Give the position of every leukocyte visible.
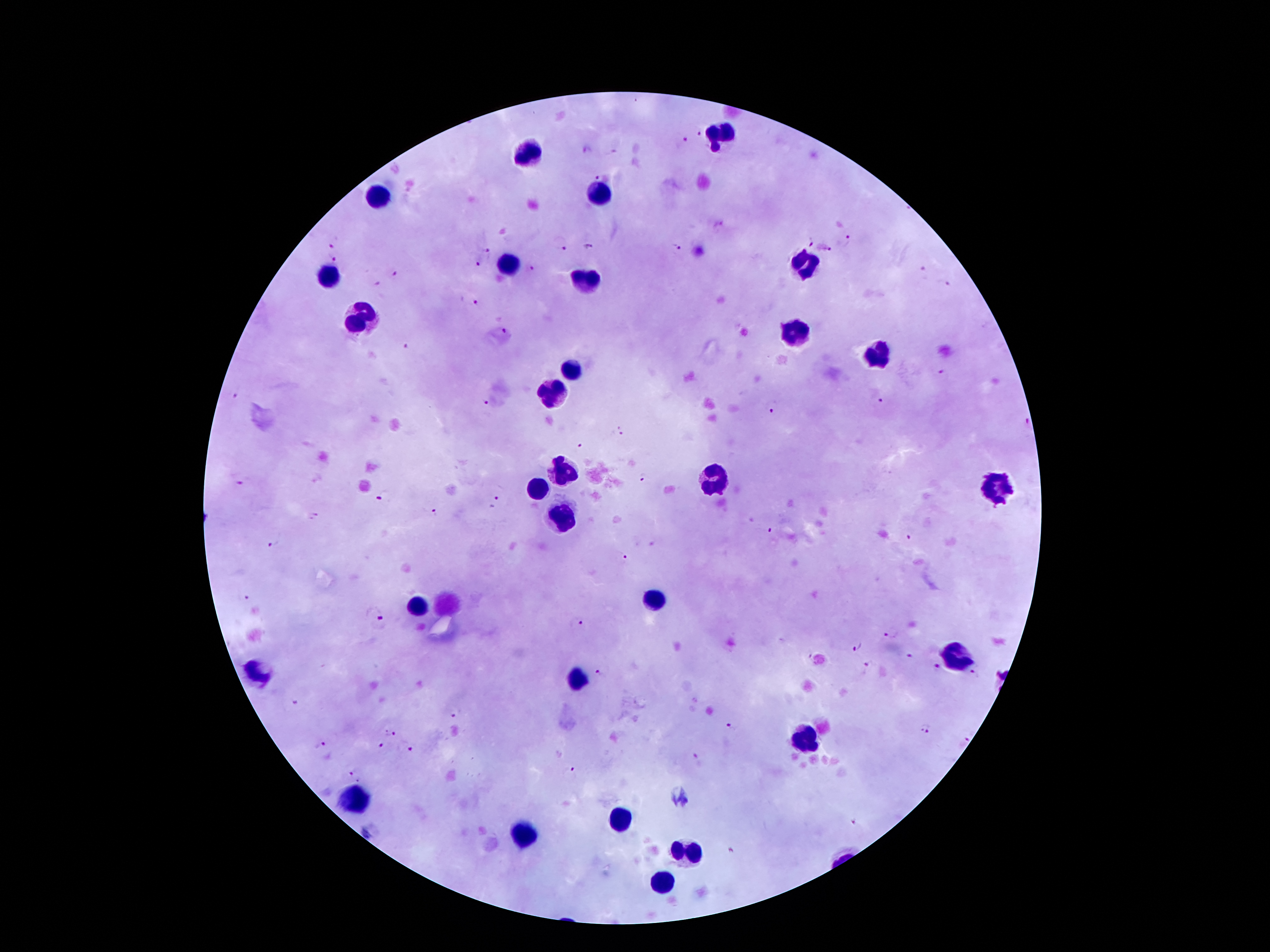
Approximate centers as [x, y] in pixels.
Leukocytes: [723, 132], [534, 152], [601, 192], [379, 196], [801, 261], [507, 262], [328, 280], [586, 282], [364, 318], [792, 335], [878, 354], [572, 369], [552, 394], [562, 470], [712, 478], [997, 488], [537, 489], [563, 521], [657, 600], [417, 608], [957, 656], [254, 675], [580, 678], [805, 738], [352, 796], [619, 819], [524, 835], [685, 851], [660, 881].

Summary:
  - Plasmodium parasite locations: [699, 132], [682, 140], [586, 150], [599, 176], [334, 240], [848, 240], [809, 245], [589, 246], [562, 248], [677, 248], [488, 251], [827, 251], [332, 258], [477, 265], [530, 267], [920, 269], [396, 273], [375, 284], [948, 285], [473, 301], [504, 330], [404, 345], [943, 373], [235, 395], [485, 401], [880, 401], [772, 411], [621, 434], [581, 446], [645, 479], [241, 481], [383, 496], [495, 503], [433, 513], [313, 517], [771, 530], [909, 538], [273, 543], [621, 557], [247, 595], [376, 612], [575, 622], [891, 633], [855, 648], [908, 656], [868, 662], [935, 667], [603, 672], [975, 674], [295, 705], [455, 711], [730, 724], [925, 728], [390, 731], [319, 746], [385, 748], [414, 748], [698, 756], [349, 768], [567, 774], [860, 820], [732, 853]
  - Patient malaria status: positive for Plasmodium falciparum
  - Field of view: one from this slide
  - Stain: Giemsa
  - Preparation: thick blood smear
  - Magnification: 100x
  - Image size: 1270×952 pixels
  - Capture: smartphone through the microscope eyepiece